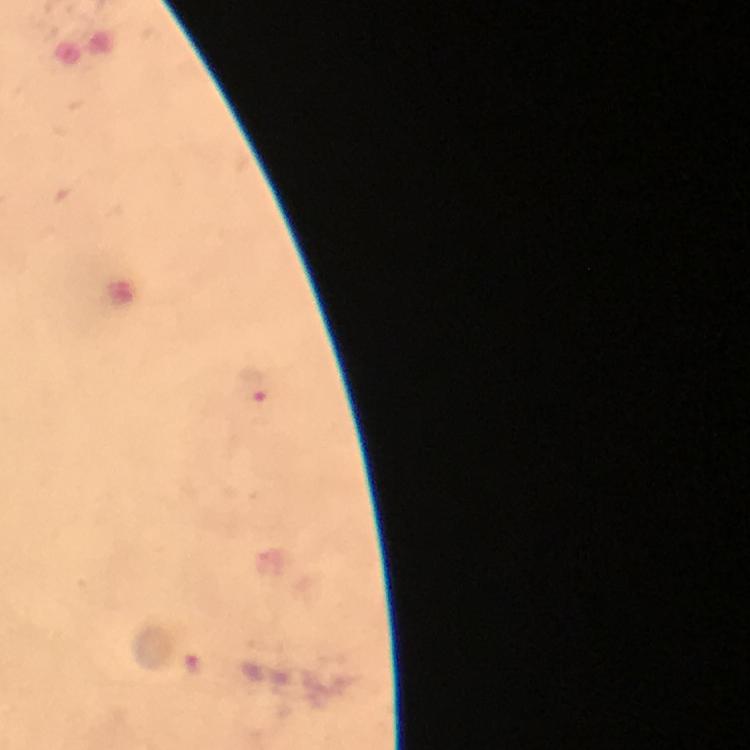
Approximate centers as (x, y) in pixels. Malaria parasite locations: (251, 385), (193, 668). From a diagnostic examination for malaria. Thick blood film. Photographed with a smartphone mounted on the microscope. 100x magnification. Immersion oil applied. Image is 750×750 pixels. A crop from one field of view. Giemsa stain.